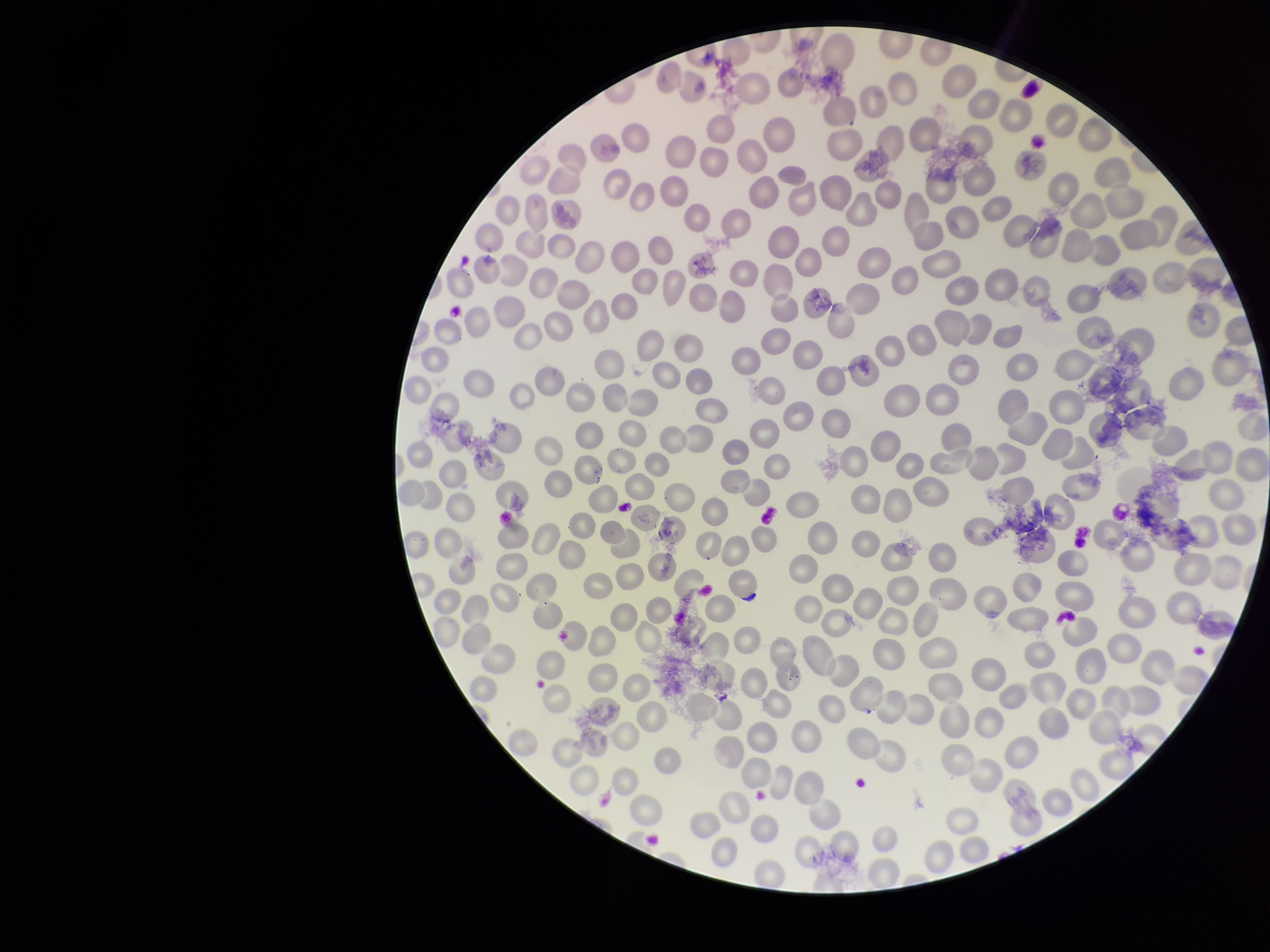
Summary:
  - Parasitized red blood cell count: 0
  - Patient malaria status: negative
  - Preparation: thin smear
  - Red blood cell count: 283
  - Image size: 1270×952 pixels
  - Parasitized red blood cells: none seen
  - Stain: Giemsa
  - Field of view: single
  - Capture: smartphone photograph through the microscope eyepiece